Classify this cell by malaria status.
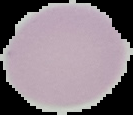

Uninfected.

{
  "preparation": "thin blood film",
  "image_size": "133×115 pixels",
  "image_type": "cell region segmented out of the field of view; surrounding area masked to black"
}